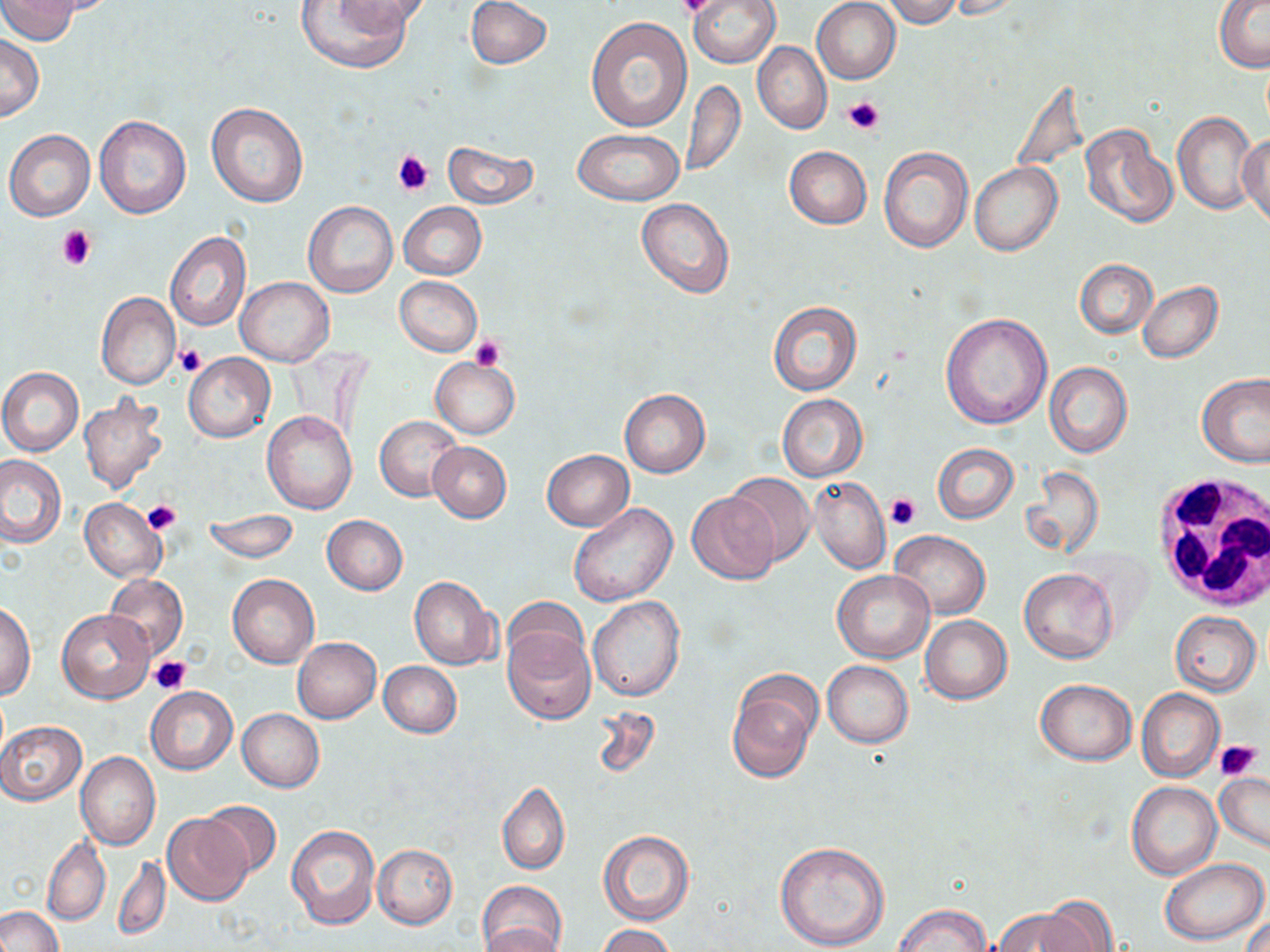 Approximate bounding boxes as [x1, y1, x2, y2] in pixels. White blood cell locations: [1148, 473, 1269, 609]. Uninfected red blood cell locations: [1, 0, 81, 43], [339, 0, 432, 34], [466, 0, 552, 69], [688, 0, 779, 68], [812, 0, 901, 83], [881, 0, 965, 28], [948, 0, 1030, 20], [1214, 0, 1269, 71], [294, 1, 415, 73], [586, 16, 692, 131], [0, 33, 44, 122], [751, 42, 831, 134], [681, 80, 746, 177], [206, 102, 309, 208], [1173, 113, 1258, 215], [94, 114, 191, 219], [1080, 123, 1178, 229], [574, 128, 684, 206], [4, 129, 95, 221], [1239, 129, 1270, 228], [441, 140, 540, 209], [878, 145, 972, 253], [784, 146, 872, 228], [970, 162, 1062, 256], [636, 197, 735, 299], [303, 202, 398, 298], [398, 202, 486, 279], [165, 231, 251, 332], [1075, 259, 1156, 338], [235, 276, 334, 366], [394, 276, 482, 356], [1137, 281, 1223, 364], [96, 293, 179, 389], [768, 301, 862, 396], [939, 312, 1051, 431], [183, 353, 275, 442], [431, 358, 519, 439], [1044, 362, 1132, 458], [0, 368, 84, 455], [1196, 373, 1270, 469], [619, 389, 710, 477], [777, 394, 867, 482], [80, 395, 168, 494], [261, 411, 358, 515], [376, 415, 463, 500], [428, 441, 512, 522], [932, 443, 1018, 523], [542, 449, 634, 530], [0, 454, 68, 549], [1018, 466, 1103, 561], [723, 472, 817, 567], [810, 476, 889, 575], [688, 491, 780, 583], [80, 499, 166, 582], [568, 502, 678, 607], [204, 512, 298, 564], [322, 514, 408, 595], [889, 530, 989, 618], [1019, 567, 1118, 664], [833, 569, 935, 662], [228, 573, 318, 668], [104, 575, 188, 659], [409, 576, 499, 671], [588, 596, 685, 701], [503, 599, 588, 676], [1, 603, 36, 700], [57, 609, 154, 703], [1169, 611, 1261, 695], [920, 615, 1012, 704], [502, 624, 596, 725], [293, 637, 381, 723], [378, 660, 461, 738], [822, 660, 913, 747], [727, 673, 820, 783], [1034, 678, 1137, 765], [146, 686, 236, 774], [1136, 688, 1223, 782], [591, 704, 660, 780], [237, 709, 324, 792], [0, 721, 86, 804], [76, 751, 160, 850], [1214, 770, 1270, 853], [1127, 781, 1221, 880], [498, 782, 570, 876], [201, 799, 281, 879], [163, 813, 253, 906], [284, 825, 379, 930], [598, 830, 693, 925], [41, 836, 111, 928], [774, 841, 890, 952], [373, 844, 457, 929], [113, 854, 170, 942], [1160, 858, 1269, 944], [479, 881, 566, 950], [1034, 898, 1121, 951], [893, 903, 991, 952], [0, 906, 64, 952], [991, 908, 1091, 951], [1241, 909, 1269, 952], [595, 924, 676, 952], [481, 926, 565, 952]. Platelet locations: [679, 0, 716, 19], [842, 96, 884, 136], [391, 148, 434, 196], [56, 226, 97, 270], [470, 335, 506, 371], [175, 346, 204, 375], [884, 492, 921, 530], [140, 501, 180, 535], [150, 656, 191, 695], [1214, 738, 1263, 781]. Slide-level diagnosis: negative for blood parasites. Thin blood smear. May-Grünwald-Giemsa stain. Captured at 1000x magnification. Optical microscopy. One field of a larger specimen. Image is 1270×952 pixels.